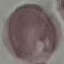
Result: negative for malaria parasites. Cell patch, automatically extracted from a larger field of view and resized to 64 × 64 pixels. Thin smear of blood. Acquired by smartphone through the microscope eyepiece. Giemsa stain.